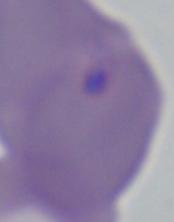
Summary:
  - Magnification: 1000x
  - Identification: Babesia
  - Modality: micrograph